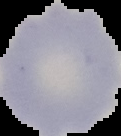

preparation = thin blood film
malaria status = uninfected
image size = 121×136 pixels
image type = segmented cell region on a black background